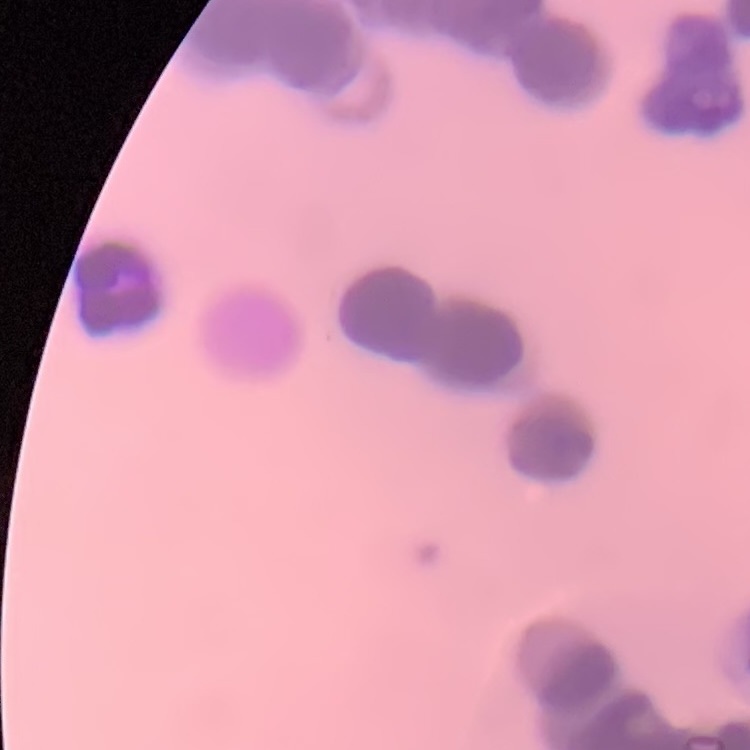

red blood cell morphology = rouleaux formation
image type = one tile cut from a larger photomicrograph
stain = Field's or Giemsa
preparation = thin peripheral smear